Outline each blood parasite and name the species.
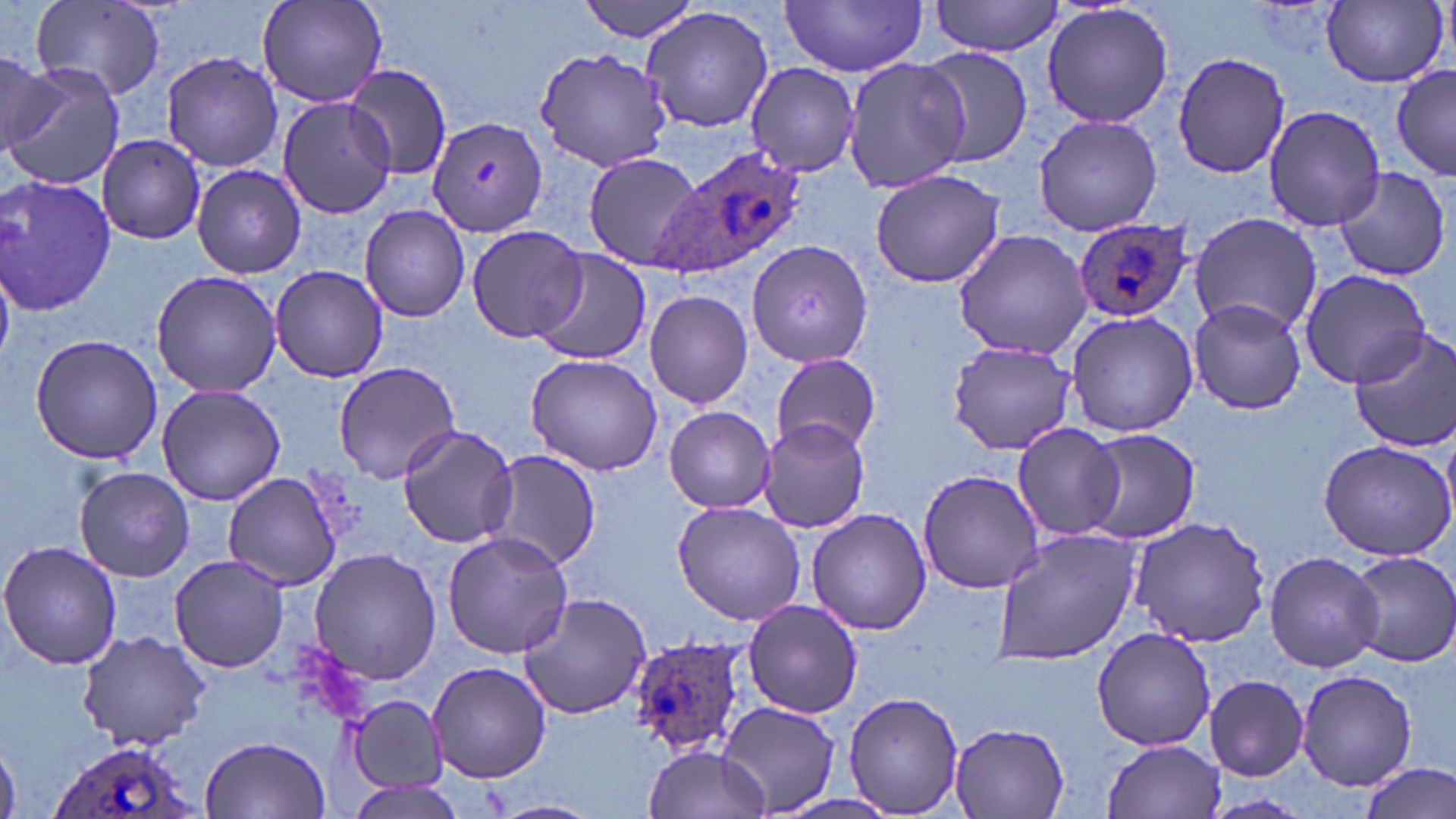

Approximate bounding boxes as named x1/y1/x2/y2 corners in pixels.
Plasmodium ovale-infected red blood cells: (x1=657, y1=143, x2=810, y2=280), (x1=1070, y1=218, x2=1194, y2=324), (x1=625, y1=633, x2=752, y2=761), (x1=47, y1=738, x2=199, y2=819).
No Plasmodium falciparum, Plasmodium malariae, Plasmodium vivax, Babesia divergens, or Trypanosoma brucei observed.

slide-level diagnosis = Plasmodium ovale
uninfected red blood cell locations = approximate bounding boxes as named x1/y1/x2/y2 corners in pixels: (x1=32, y1=0, x2=166, y2=101), (x1=258, y1=0, x2=388, y2=110), (x1=578, y1=0, x2=701, y2=43), (x1=930, y1=0, x2=1064, y2=56), (x1=781, y1=1, x2=929, y2=76), (x1=1322, y1=1, x2=1447, y2=88), (x1=1040, y1=2, x2=1174, y2=130), (x1=640, y1=6, x2=774, y2=135), (x1=534, y1=45, x2=672, y2=171), (x1=914, y1=46, x2=1033, y2=168), (x1=159, y1=51, x2=286, y2=172), (x1=1171, y1=51, x2=1291, y2=178), (x1=0, y1=52, x2=62, y2=154), (x1=840, y1=55, x2=969, y2=197), (x1=4, y1=62, x2=123, y2=189), (x1=745, y1=62, x2=862, y2=179), (x1=344, y1=65, x2=452, y2=182), (x1=1392, y1=65, x2=1456, y2=182), (x1=279, y1=96, x2=396, y2=219), (x1=1263, y1=103, x2=1386, y2=231), (x1=1032, y1=115, x2=1164, y2=237), (x1=428, y1=116, x2=548, y2=239), (x1=98, y1=134, x2=206, y2=244), (x1=581, y1=150, x2=703, y2=274), (x1=190, y1=164, x2=306, y2=278), (x1=1331, y1=164, x2=1451, y2=281), (x1=869, y1=168, x2=1005, y2=289), (x1=1, y1=175, x2=117, y2=319), (x1=359, y1=205, x2=471, y2=321), (x1=1189, y1=213, x2=1322, y2=336), (x1=465, y1=224, x2=589, y2=345), (x1=951, y1=229, x2=1094, y2=360), (x1=748, y1=240, x2=874, y2=368), (x1=534, y1=252, x2=651, y2=368), (x1=271, y1=266, x2=387, y2=383), (x1=1299, y1=268, x2=1435, y2=391), (x1=149, y1=269, x2=282, y2=396), (x1=644, y1=289, x2=754, y2=410), (x1=1186, y1=299, x2=1309, y2=416), (x1=1065, y1=311, x2=1201, y2=437), (x1=1348, y1=327, x2=1456, y2=453), (x1=28, y1=333, x2=163, y2=466), (x1=947, y1=339, x2=1081, y2=456), (x1=771, y1=352, x2=882, y2=455), (x1=523, y1=353, x2=664, y2=476), (x1=333, y1=360, x2=462, y2=483), (x1=156, y1=385, x2=286, y2=506), (x1=664, y1=406, x2=777, y2=512), (x1=760, y1=416, x2=870, y2=532), (x1=1013, y1=423, x2=1125, y2=542), (x1=397, y1=426, x2=519, y2=550), (x1=1083, y1=428, x2=1201, y2=544), (x1=1318, y1=440, x2=1456, y2=562), (x1=483, y1=449, x2=602, y2=572), (x1=75, y1=466, x2=195, y2=582), (x1=917, y1=468, x2=1043, y2=593), (x1=223, y1=472, x2=341, y2=590), (x1=40, y1=474, x2=162, y2=611), (x1=671, y1=499, x2=807, y2=625), (x1=805, y1=508, x2=932, y2=635), (x1=1127, y1=515, x2=1274, y2=648), (x1=990, y1=527, x2=1139, y2=664), (x1=441, y1=530, x2=574, y2=661), (x1=0, y1=539, x2=122, y2=671), (x1=306, y1=546, x2=443, y2=686), (x1=1345, y1=550, x2=1456, y2=668), (x1=1263, y1=551, x2=1385, y2=672), (x1=169, y1=555, x2=291, y2=674), (x1=515, y1=593, x2=654, y2=721), (x1=742, y1=599, x2=863, y2=718), (x1=1091, y1=626, x2=1217, y2=752), (x1=77, y1=629, x2=210, y2=751), (x1=429, y1=661, x2=551, y2=783), (x1=1296, y1=669, x2=1419, y2=790), (x1=1204, y1=674, x2=1309, y2=780), (x1=842, y1=691, x2=964, y2=815), (x1=344, y1=693, x2=448, y2=795), (x1=720, y1=702, x2=839, y2=816), (x1=949, y1=721, x2=1072, y2=816), (x1=201, y1=735, x2=329, y2=818), (x1=1103, y1=739, x2=1227, y2=818), (x1=0, y1=740, x2=23, y2=819), (x1=641, y1=745, x2=769, y2=819), (x1=1360, y1=762, x2=1454, y2=819), (x1=485, y1=798, x2=600, y2=819)
image size = 1456×819 pixels
stain = May-Grünwald-Giemsa
preparation = thin blood smear
field of view = single
magnification = 1000x
modality = optical microscopy